Comment on the morphology of the erythrocytes.
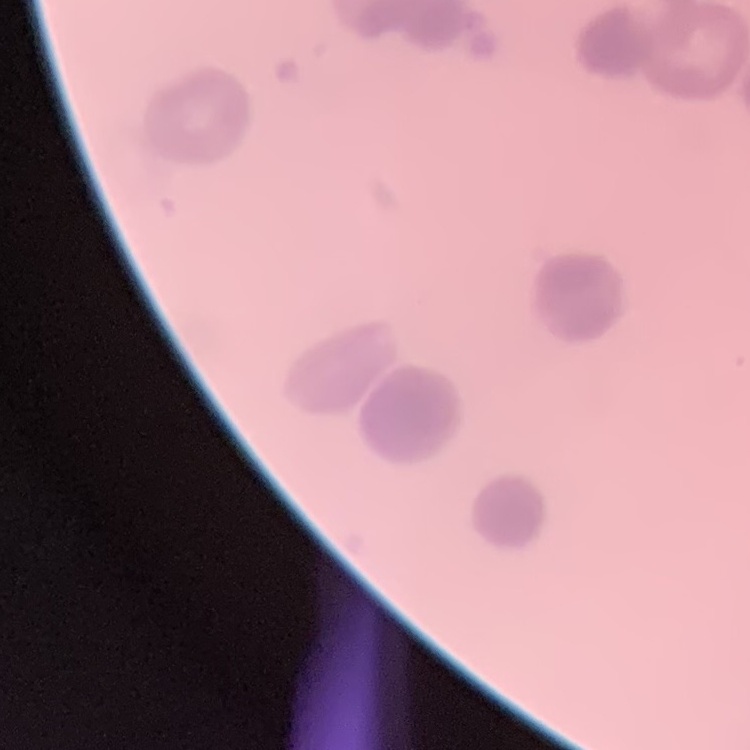

Rouleaux formation.

Thin blood film. Stained with either Field's or Giemsa. One tile cut from a larger photomicrograph.